Locate and identify every blood parasite.
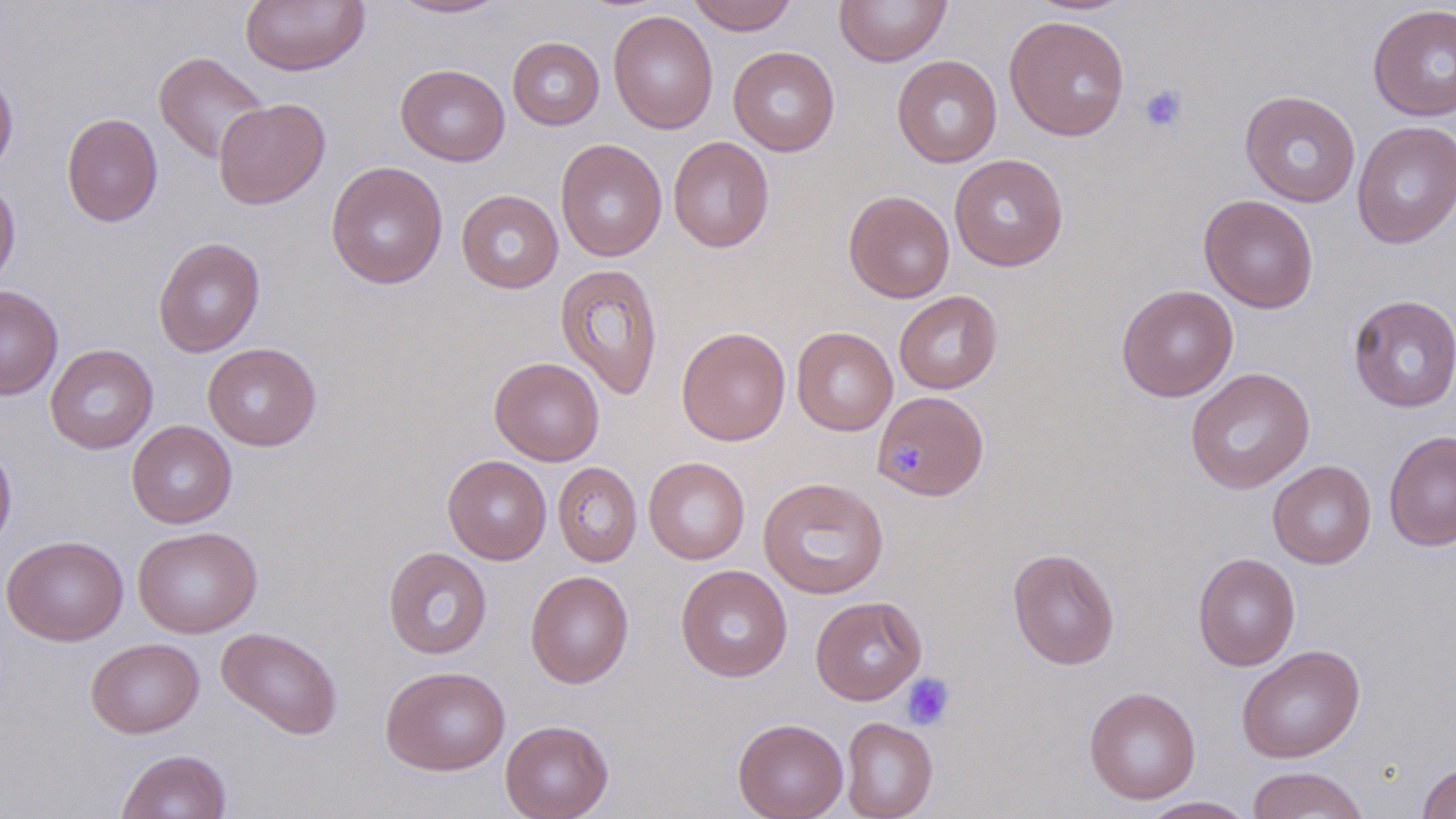

No blood parasites observed.

Summary:
  - Coordinate format: approximate bounding boxes as [x1, y1, x2, y2] in pixels
  - Platelet locations: [1139, 83, 1189, 134], [893, 439, 932, 482], [900, 672, 956, 731]
  - Uninfected red blood cell locations: [239, 0, 370, 76], [389, 0, 509, 19], [686, 0, 799, 35], [833, 0, 952, 67], [1025, 0, 1137, 15], [1367, 3, 1456, 122], [607, 10, 719, 134], [1004, 15, 1130, 141], [507, 36, 605, 130], [728, 46, 840, 156], [153, 51, 269, 164], [892, 55, 1002, 168], [396, 64, 510, 165], [0, 65, 19, 177], [1240, 90, 1361, 207], [213, 98, 331, 209], [61, 112, 163, 227], [1351, 120, 1456, 249], [667, 136, 775, 253], [555, 138, 667, 262], [949, 153, 1068, 271], [326, 161, 448, 289], [0, 177, 21, 290], [456, 189, 563, 293], [843, 190, 955, 302], [1198, 194, 1319, 313], [152, 237, 265, 357], [555, 263, 664, 400], [1116, 284, 1238, 402], [0, 285, 63, 400], [894, 290, 1003, 394], [1347, 294, 1456, 413], [676, 326, 791, 446], [791, 327, 898, 435], [203, 342, 322, 451], [45, 344, 158, 454], [489, 356, 605, 465], [1185, 367, 1315, 494], [878, 397, 996, 501], [126, 421, 237, 528], [1384, 429, 1456, 551], [0, 436, 18, 557], [442, 455, 552, 564], [644, 457, 750, 564], [1268, 460, 1376, 569], [552, 462, 642, 566], [758, 476, 889, 599], [132, 525, 262, 638], [1, 535, 129, 645], [383, 547, 492, 659], [1007, 547, 1121, 670], [1192, 552, 1300, 671], [676, 564, 792, 682], [525, 570, 634, 688], [810, 596, 927, 704], [216, 626, 343, 739], [86, 638, 204, 738], [1236, 644, 1365, 763], [379, 665, 511, 775], [1084, 686, 1201, 805], [733, 717, 848, 819], [840, 717, 938, 819], [500, 719, 614, 819], [116, 748, 232, 819], [1416, 762, 1456, 819], [1246, 766, 1369, 818], [1138, 796, 1258, 818]
  - Slide-level diagnosis: negative for blood parasites
  - Stain: May-Grünwald-Giemsa
  - Field of view: one of a larger specimen
  - Preparation: thin blood film
  - Image size: 1456×819 pixels
  - Magnification: 1000x
  - Modality: optical microscopy